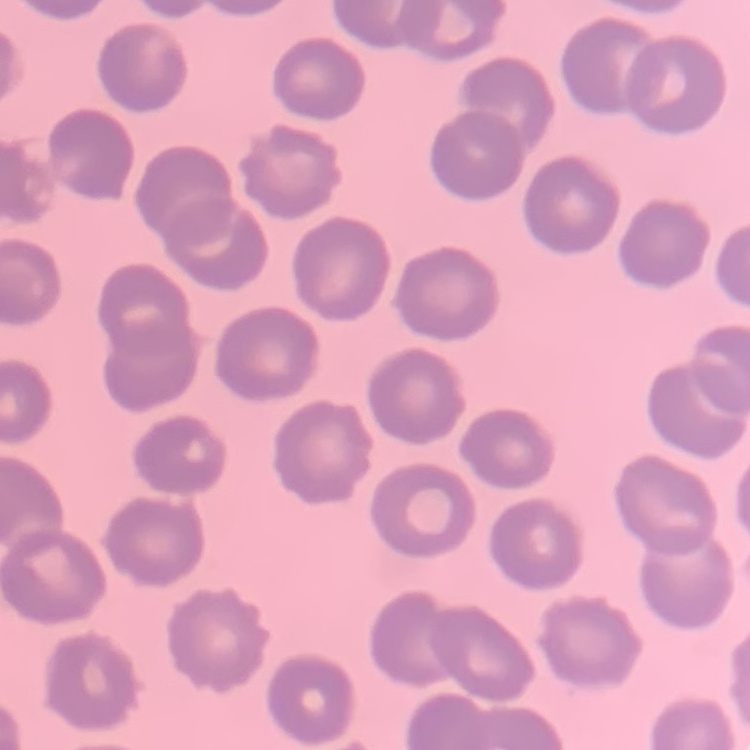

Summary:
  - Erythrocyte morphology: no rouleaux formation
  - Image type: one tile cut from a larger photomicrograph
  - Stain: Field's or Giemsa
  - Preparation: thin peripheral smear